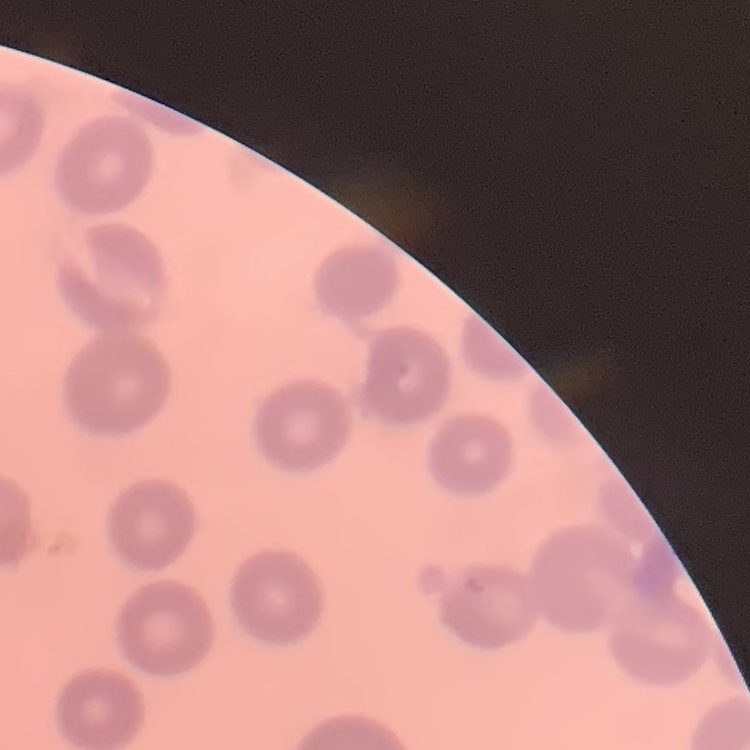

{
  "erythrocyte_morphology": "no rouleaux formation",
  "preparation": "thin peripheral smear",
  "image_type": "square crop of a larger photomicrograph",
  "stain": "Field's or Giemsa"
}